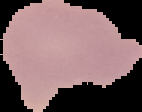
Summary:
  - Result: no malaria parasites detected
  - Preparation: thin blood smear
  - Image type: cell region segmented out of the field of view; surrounding area masked to black
  - Image size: 142×112 pixels